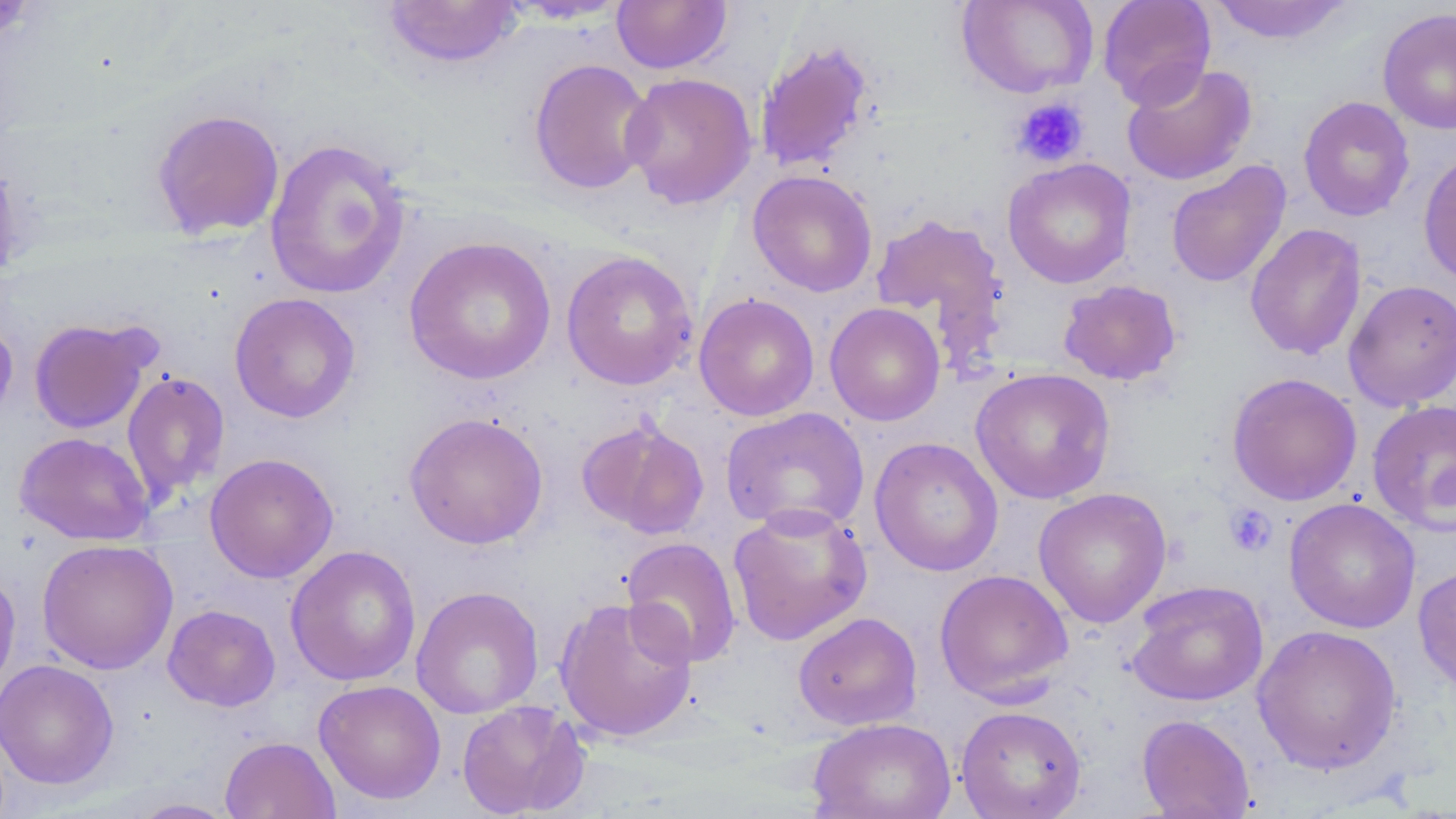
Approximate bounding boxes as (x1, y1, x2, y2) in pixels. Uninfected red blood cell locations: (957, 0, 1098, 99), (1097, 0, 1217, 109), (1207, 0, 1354, 45), (0, 1, 41, 45), (381, 1, 524, 70), (612, 1, 732, 73), (1377, 7, 1456, 135), (754, 39, 876, 174), (528, 58, 656, 196), (1121, 61, 1258, 186), (620, 71, 757, 210), (1298, 95, 1415, 222), (150, 108, 286, 240), (264, 138, 412, 300), (1418, 150, 1456, 287), (1003, 158, 1137, 288), (1166, 161, 1291, 288), (747, 170, 878, 297), (869, 211, 1008, 355), (1245, 223, 1367, 361), (403, 236, 556, 386), (560, 250, 698, 391), (1058, 279, 1182, 386), (1343, 279, 1456, 412), (229, 292, 361, 423), (694, 292, 819, 421), (825, 303, 945, 426), (0, 317, 18, 432), (28, 317, 158, 434), (970, 367, 1116, 504), (121, 370, 230, 504), (1226, 372, 1363, 506), (1367, 400, 1456, 535), (720, 407, 869, 535), (404, 411, 548, 550), (576, 416, 710, 540), (15, 431, 153, 546), (869, 436, 1003, 576), (204, 452, 339, 583), (1033, 487, 1172, 628), (1283, 497, 1421, 634), (727, 503, 872, 646), (620, 537, 742, 668), (36, 539, 179, 674), (285, 544, 422, 686), (1413, 561, 1456, 696), (0, 568, 21, 700), (933, 568, 1074, 704), (1126, 580, 1269, 707), (411, 586, 544, 719), (554, 595, 698, 743), (162, 604, 281, 712), (793, 612, 922, 730), (1252, 624, 1402, 775), (0, 659, 119, 791), (313, 679, 446, 805), (456, 700, 590, 818), (956, 705, 1086, 819), (1136, 714, 1256, 818), (807, 717, 957, 819), (220, 736, 339, 819), (125, 798, 241, 818). Platelet locations: (1011, 96, 1089, 167), (1224, 504, 1277, 557). Slide-level diagnosis: no evidence of blood parasites. Captured at 1000x magnification. Thin blood smear. May-Grünwald-Giemsa-stained preparation. Single field of view. Image is 1456×819 pixels. Optical microscopy.